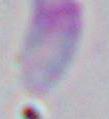

Summary:
  - Identification: Toxoplasma gondii
  - Modality: micrograph
  - Magnification: 1000x